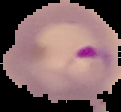
image size = 121×112 pixels
preparation = thin blood smear
result = Plasmodium parasites detected
image type = cell region segmented out of the field of view; surrounding area masked to black